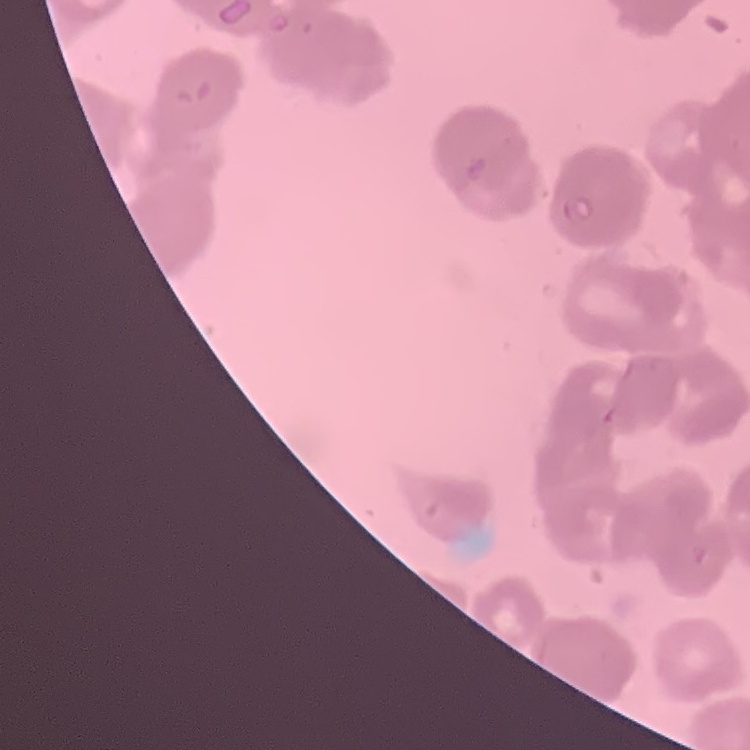
Summary:
  - Erythrocyte morphology: rouleaux formation
  - Preparation: thin blood film
  - Stain: Field's or Giemsa
  - Image type: square crop of a larger photomicrograph